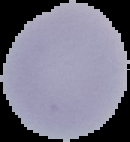

Summary:
  - Preparation: thin blood smear
  - Image size: 130×142 pixels
  - Image type: cell region segmented out of the field of view; surrounding area masked to black
  - Result: no Plasmodium parasites detected